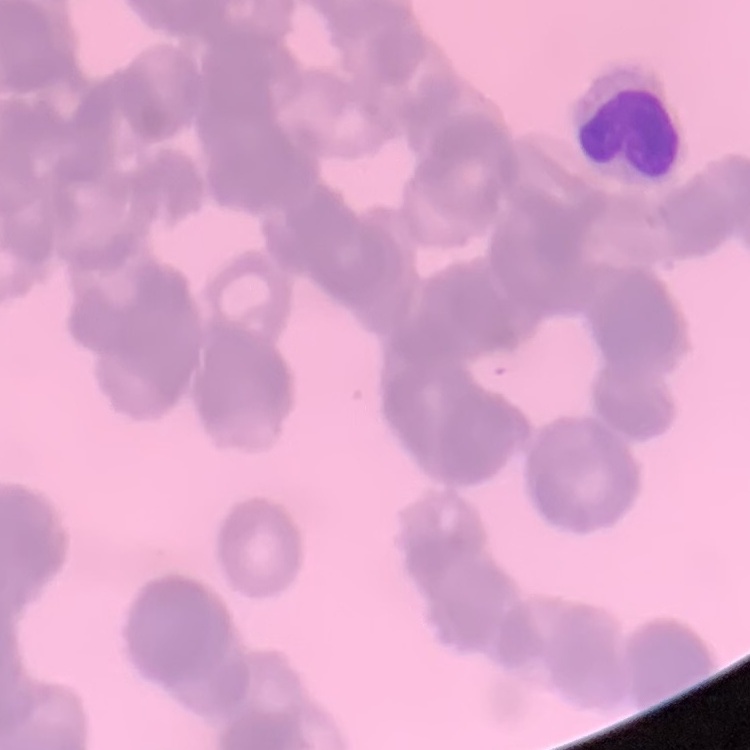

The red blood cells show rouleaux formation. Square crop of a larger photomicrograph. Field's or Giemsa stain. Thin peripheral smear.